State which parasite is depicted.
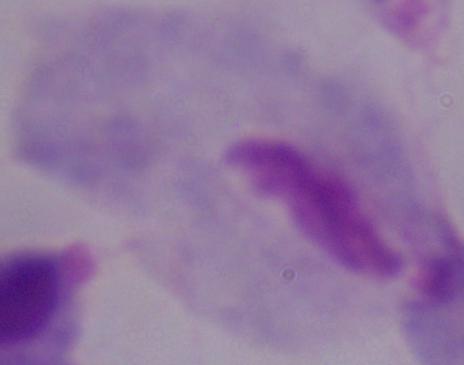

A trichomonad.

Photomicrograph. 1000x magnification.